Name the parasite shown.
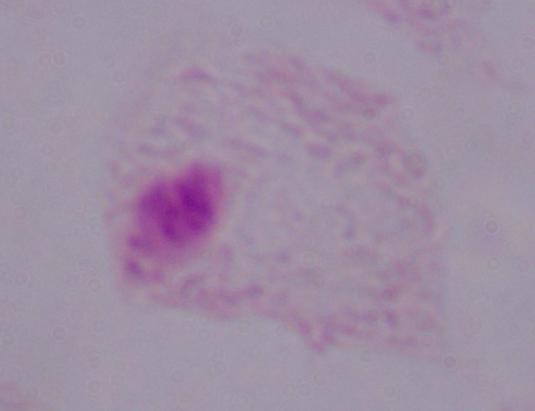

This is a trichomonad.

Photomicrograph. Captured at 1000x magnification.